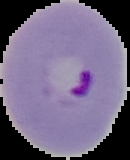
Summary:
  - Malaria status: parasitized
  - Image size: 130×160 pixels
  - Preparation: thin blood film
  - Image type: cell region segmented out of the field of view; surrounding area masked to black